Identify the preparation type.
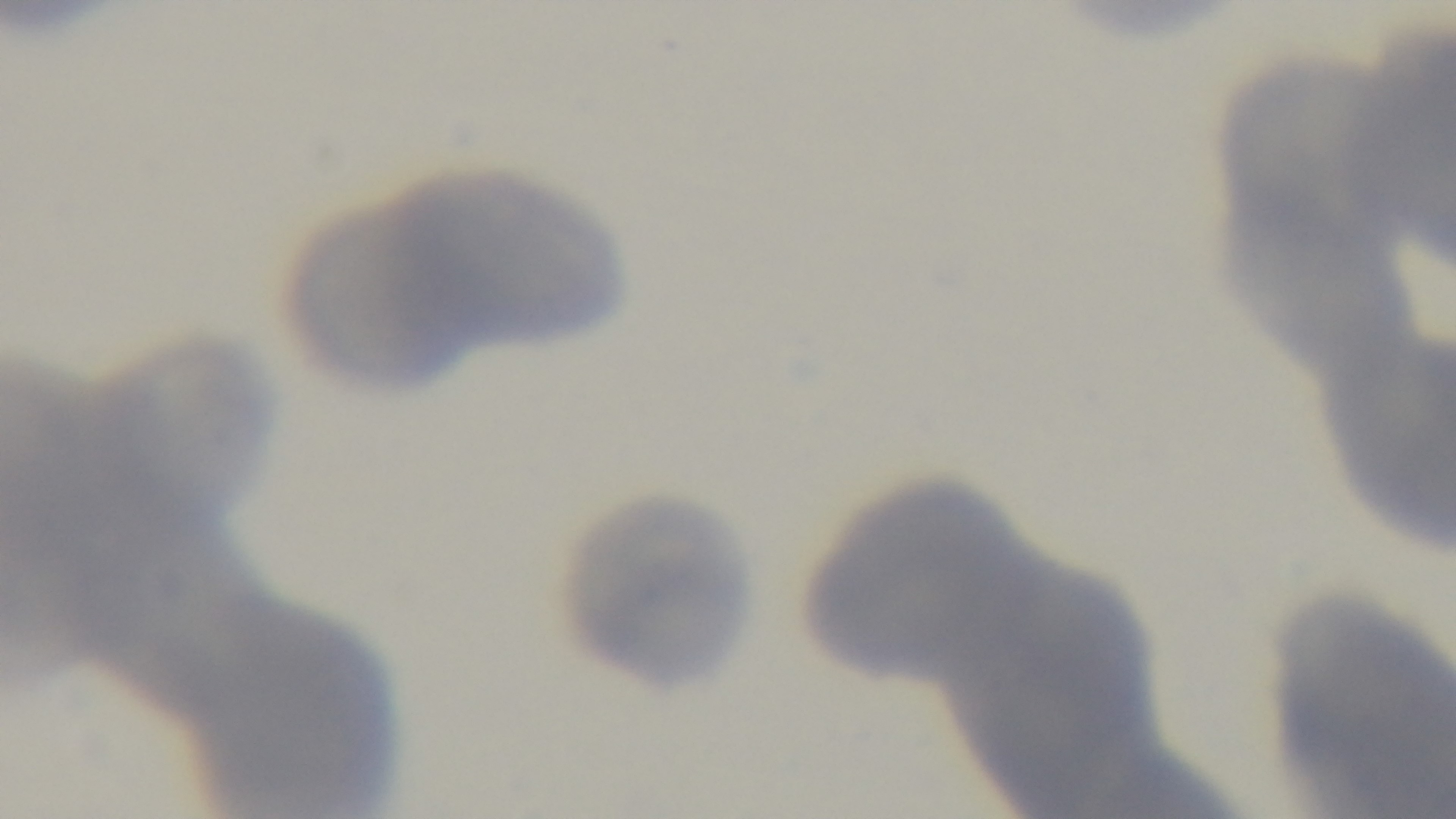
It is a thin blood film.

Light microscopy. Malaria status: uninfected. Mounted 4K digital camera. Giemsa-stained. Oil-immersion objective, 100x. One field from the slide.